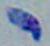 Photomicrograph. 1000x magnification. Toxoplasma gondii is seen.